Identify the parasite.
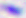

Toxoplasma gondii.

Captured at 400x magnification. Micrograph.